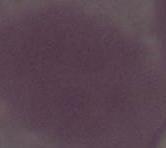

Summary:
  - Modality: micrograph
  - Identification: red blood cell
  - Magnification: 1000x